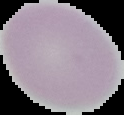

image type = cell region segmented out of the field of view; surrounding area masked to black
image size = 124×115 pixels
preparation = thin blood film
malaria status = uninfected